Give the position of every leukocyte visible.
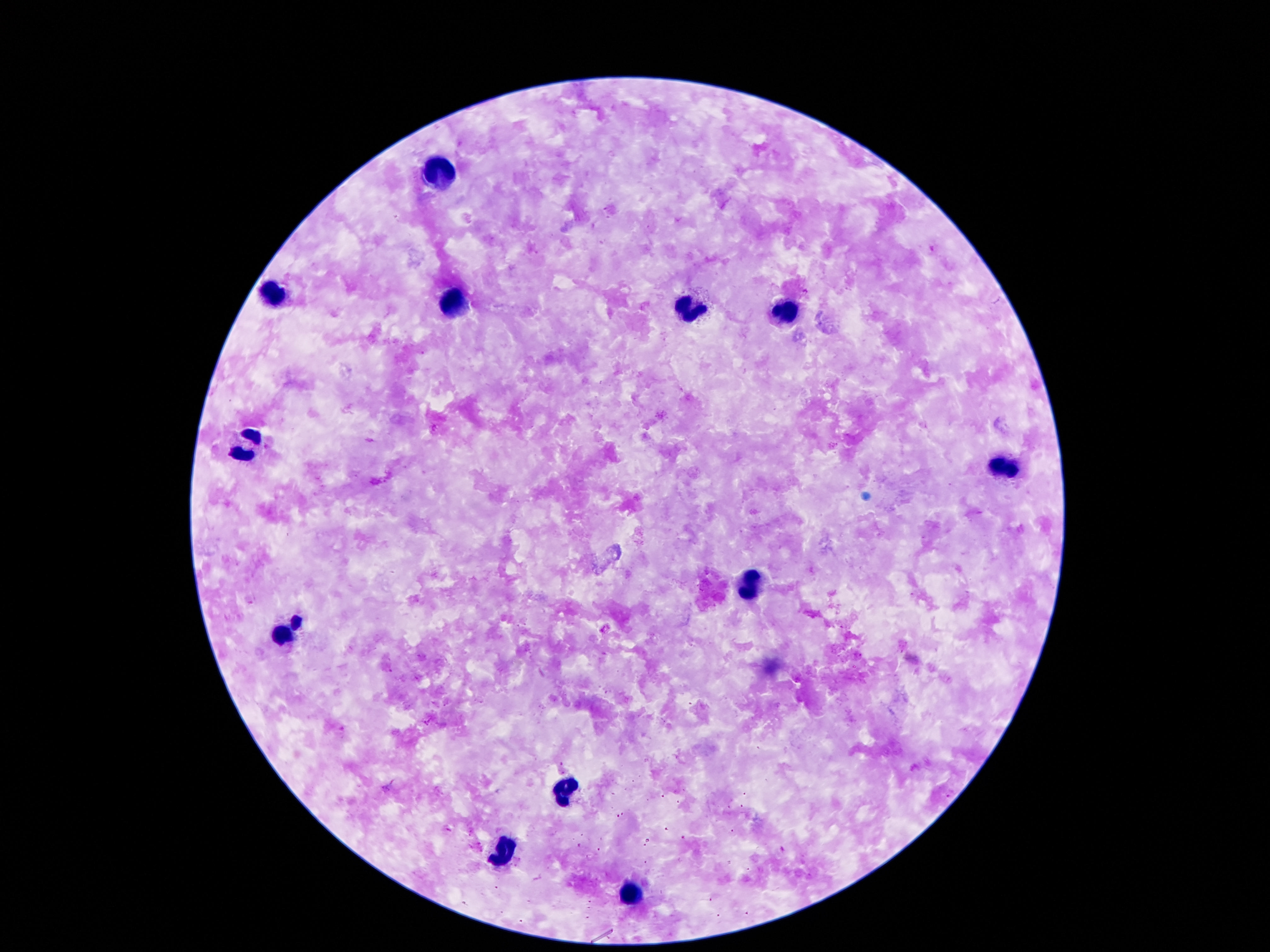

Approximate centers as (x, y) in pixels.
Leukocytes: (435, 178), (270, 294), (452, 302), (688, 305), (780, 311), (248, 446), (1010, 464), (750, 582), (284, 629), (563, 793), (501, 852), (628, 898).

patient_malaria_status: not infected
image_size: 1270×952 pixels
stain: Giemsa
magnification: 100x
capture: smartphone camera through the microscope eyepiece
preparation: thick blood film
field_of_view: single